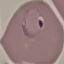

Summary:
  - Malaria status: parasitized
  - Preparation: thin blood film
  - Image type: cell patch, automatically extracted from a larger field of view and resized to 64 × 64 pixels
  - Stain: Giemsa
  - Capture: smartphone through the microscope eyepiece